Classify this cell by malaria status.
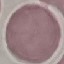

Uninfected.

Summary:
  - Capture: smartphone camera at the microscope eyepiece
  - Stain: Giemsa
  - Preparation: thin smear
  - Image type: cell patch, automatically extracted from a larger field of view and resized to 64 × 64 pixels